Assess the morphology of the red blood cells.
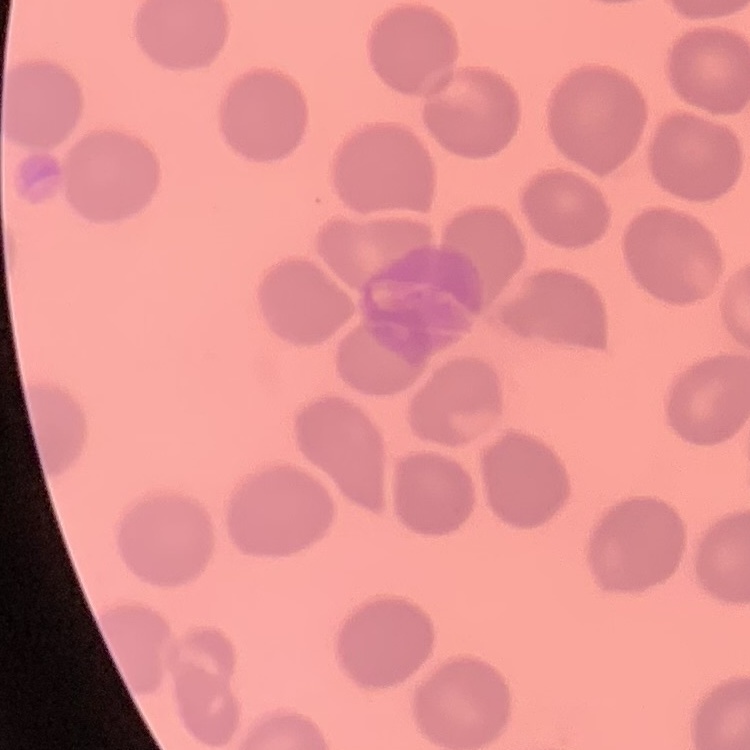

No rouleaux formation.

preparation = thin blood smear
stain = Field's or Giemsa
image type = square crop of a larger photomicrograph